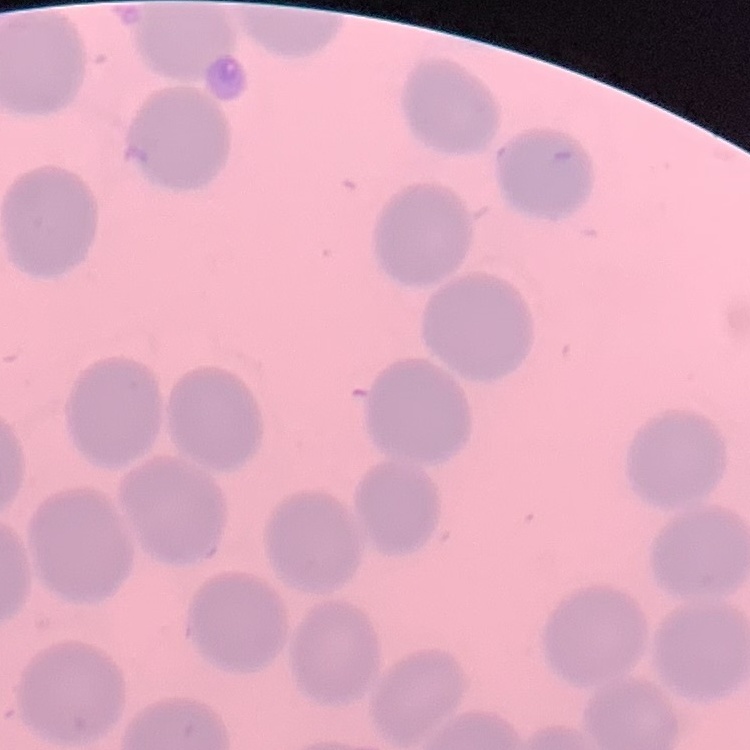

Summary:
  - Red blood cell morphology: no rouleaux formation
  - Preparation: thin blood film
  - Image type: one tile cut from a larger photomicrograph
  - Stain: Field's or Giemsa